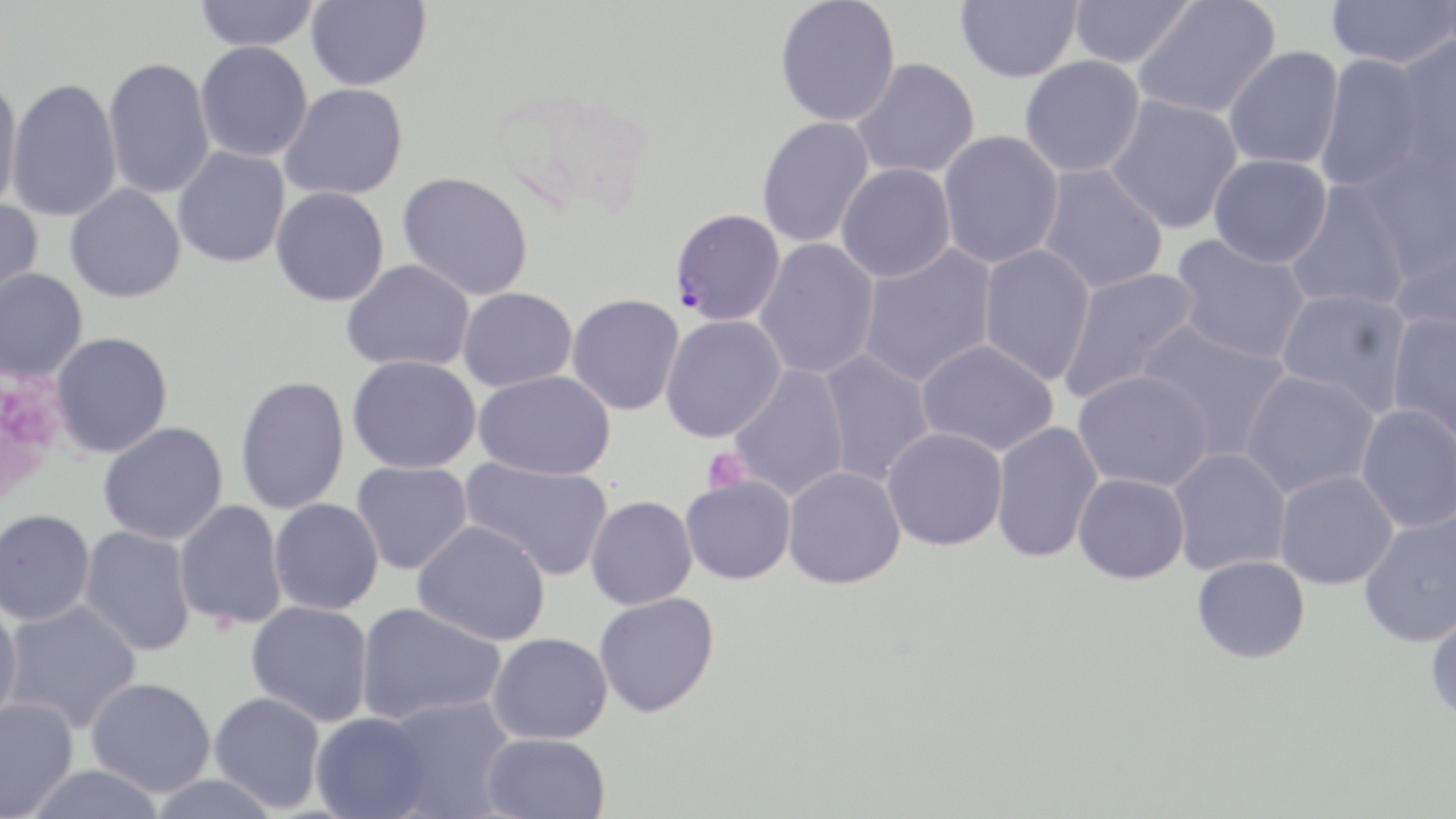

Approximate bounding boxes as named x1/y1/x2/y2 corners in pixels. Platelet locations: (x1=0, y1=370, x2=68, y2=505), (x1=702, y1=448, x2=749, y2=494). Plasmodium falciparum-infected red blood cell locations: (x1=670, y1=208, x2=785, y2=327). Uninfected red blood cell locations: (x1=193, y1=0, x2=320, y2=51), (x1=305, y1=0, x2=431, y2=91), (x1=955, y1=0, x2=1082, y2=83), (x1=1134, y1=0, x2=1280, y2=119), (x1=1325, y1=0, x2=1455, y2=69), (x1=774, y1=1, x2=901, y2=127), (x1=1067, y1=1, x2=1195, y2=69), (x1=1393, y1=35, x2=1456, y2=174), (x1=195, y1=41, x2=312, y2=162), (x1=1224, y1=46, x2=1344, y2=170), (x1=1316, y1=54, x2=1428, y2=193), (x1=1019, y1=56, x2=1146, y2=178), (x1=102, y1=58, x2=215, y2=200), (x1=852, y1=58, x2=980, y2=180), (x1=0, y1=73, x2=25, y2=218), (x1=5, y1=78, x2=123, y2=221), (x1=279, y1=84, x2=408, y2=201), (x1=1104, y1=95, x2=1243, y2=234), (x1=756, y1=116, x2=875, y2=249), (x1=938, y1=130, x2=1064, y2=269), (x1=1355, y1=143, x2=1455, y2=281), (x1=172, y1=146, x2=290, y2=269), (x1=1208, y1=154, x2=1332, y2=268), (x1=836, y1=163, x2=957, y2=283), (x1=1035, y1=164, x2=1170, y2=294), (x1=397, y1=171, x2=534, y2=301), (x1=1285, y1=181, x2=1409, y2=313), (x1=65, y1=183, x2=186, y2=303), (x1=270, y1=187, x2=390, y2=307), (x1=0, y1=199, x2=44, y2=315), (x1=1390, y1=227, x2=1456, y2=338), (x1=1171, y1=235, x2=1312, y2=364), (x1=754, y1=238, x2=880, y2=379), (x1=857, y1=244, x2=998, y2=388), (x1=977, y1=244, x2=1096, y2=385), (x1=341, y1=259, x2=475, y2=372), (x1=0, y1=267, x2=89, y2=382), (x1=1058, y1=267, x2=1202, y2=404), (x1=457, y1=288, x2=576, y2=392), (x1=1275, y1=288, x2=1413, y2=416), (x1=566, y1=294, x2=685, y2=416), (x1=1386, y1=313, x2=1456, y2=448), (x1=660, y1=315, x2=785, y2=443), (x1=1135, y1=319, x2=1293, y2=462), (x1=50, y1=332, x2=173, y2=458), (x1=916, y1=338, x2=1060, y2=456), (x1=817, y1=349, x2=935, y2=486), (x1=347, y1=355, x2=481, y2=474), (x1=728, y1=364, x2=850, y2=502), (x1=1240, y1=369, x2=1379, y2=498), (x1=473, y1=370, x2=616, y2=480), (x1=1072, y1=370, x2=1213, y2=492), (x1=234, y1=375, x2=350, y2=515), (x1=1355, y1=404, x2=1456, y2=533), (x1=98, y1=422, x2=229, y2=546), (x1=990, y1=422, x2=1104, y2=562), (x1=882, y1=427, x2=1008, y2=551), (x1=1167, y1=448, x2=1291, y2=575), (x1=460, y1=456, x2=614, y2=581), (x1=352, y1=461, x2=473, y2=575), (x1=782, y1=466, x2=906, y2=589), (x1=1274, y1=471, x2=1398, y2=589), (x1=1073, y1=473, x2=1190, y2=584), (x1=679, y1=475, x2=795, y2=585), (x1=585, y1=496, x2=697, y2=610), (x1=268, y1=498, x2=384, y2=615), (x1=173, y1=500, x2=287, y2=630), (x1=0, y1=509, x2=95, y2=626), (x1=1358, y1=509, x2=1456, y2=647), (x1=413, y1=520, x2=551, y2=646), (x1=78, y1=526, x2=196, y2=657), (x1=1192, y1=555, x2=1310, y2=663), (x1=594, y1=592, x2=719, y2=717), (x1=2, y1=600, x2=142, y2=734), (x1=1425, y1=600, x2=1456, y2=724), (x1=246, y1=601, x2=374, y2=727), (x1=355, y1=602, x2=506, y2=726), (x1=0, y1=605, x2=23, y2=730), (x1=487, y1=632, x2=612, y2=744), (x1=86, y1=677, x2=216, y2=797), (x1=209, y1=691, x2=327, y2=813), (x1=381, y1=696, x2=517, y2=818), (x1=0, y1=697, x2=79, y2=818), (x1=310, y1=712, x2=432, y2=819), (x1=479, y1=732, x2=611, y2=819), (x1=22, y1=764, x2=168, y2=819), (x1=146, y1=774, x2=281, y2=819). Slide-level diagnosis: Plasmodium falciparum. Optical microscopy. Thin blood smear. Image is 1456×819 pixels. Single field of view. May-Grünwald-Giemsa stain. Captured at 1000x magnification.